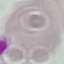
Summary:
  - Result: no malaria parasites detected
  - Preparation: thin blood film
  - Capture: smartphone camera at the microscope eyepiece
  - Image type: cell patch, automatically extracted from a larger field of view and resized to 64 × 64 pixels
  - Stain: Giemsa